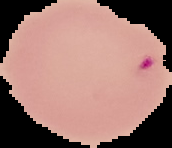

image type = segmented cell region with the area outside set to black
malaria status = parasitized
preparation = thin blood film
image size = 172×148 pixels